State which cell type is depicted.
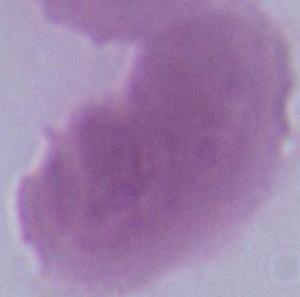
An erythrocyte.

Photomicrograph. Captured at 1000x magnification.